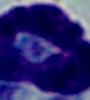
Photomicrograph. A leukocyte is shown. 1000x magnification.